Locate every uninfected red blood cell.
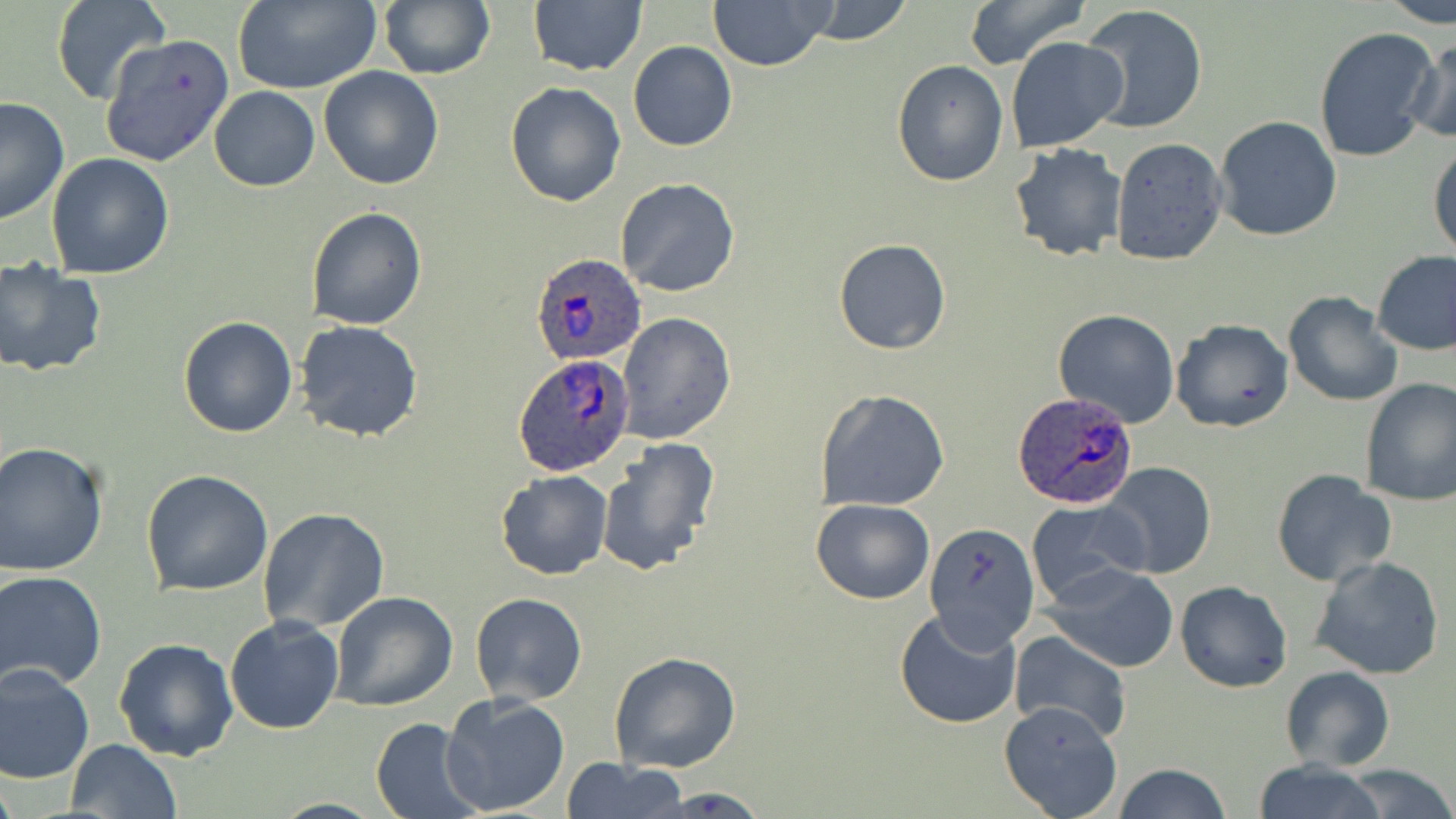

Approximate bounding boxes as (x1, y1, x2, y2) in pixels.
Uninfected red blood cells: (53, 0, 171, 107), (231, 0, 382, 94), (378, 0, 494, 81), (708, 0, 834, 71), (797, 0, 916, 47), (963, 0, 1086, 70), (1379, 0, 1456, 26), (528, 1, 647, 76), (1081, 3, 1207, 136), (1313, 27, 1441, 165), (103, 31, 234, 165), (1004, 35, 1127, 153), (1405, 35, 1456, 144), (627, 41, 739, 151), (892, 59, 1009, 186), (319, 65, 445, 189), (505, 80, 628, 207), (209, 87, 320, 191), (1, 98, 70, 225), (1214, 116, 1343, 242), (1109, 138, 1229, 266), (1427, 139, 1456, 261), (1007, 142, 1127, 263), (46, 153, 176, 279), (615, 178, 741, 299), (305, 207, 427, 331), (833, 237, 951, 353), (1372, 251, 1456, 356), (0, 258, 107, 378), (1282, 291, 1403, 407), (1053, 309, 1179, 428), (618, 312, 735, 443), (178, 314, 301, 438), (1170, 319, 1293, 434), (293, 321, 424, 443), (1358, 379, 1456, 505), (816, 387, 950, 512), (595, 438, 721, 578), (0, 442, 109, 577), (1100, 461, 1217, 580), (141, 469, 273, 596), (495, 469, 613, 580), (1271, 469, 1395, 587), (809, 498, 935, 604), (1025, 499, 1148, 609), (258, 507, 389, 632), (922, 521, 1040, 651), (1306, 555, 1447, 680), (1043, 562, 1178, 673), (0, 570, 106, 690), (1174, 579, 1293, 692), (332, 592, 459, 711), (470, 592, 587, 707), (232, 608, 451, 724), (894, 608, 1023, 730), (224, 615, 346, 734), (1008, 629, 1130, 745), (113, 636, 240, 761), (610, 650, 741, 774), (0, 661, 96, 783), (1279, 666, 1396, 772), (438, 693, 571, 816), (998, 700, 1124, 818), (369, 719, 483, 817), (65, 739, 181, 819), (562, 758, 691, 817), (1249, 759, 1390, 819), (1341, 763, 1455, 819), (1109, 764, 1235, 819), (646, 788, 774, 818).

Plasmodium ovale-infected red blood cell locations: (528, 252, 645, 367), (517, 356, 633, 475), (1013, 393, 1138, 509). Slide-level diagnosis: Plasmodium ovale. Thin blood film. One field of a larger specimen. 1000x magnification. Image is 1456×819 pixels. Light microscopy. May-Grünwald-Giemsa-stained preparation.